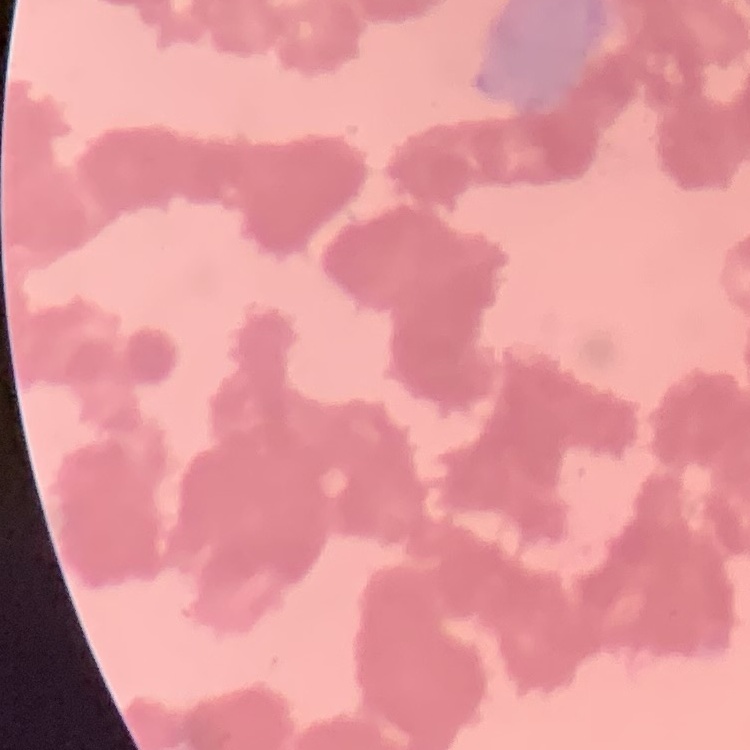

The red blood cells show rouleaux formation. Thin blood film. Stained with either Field's or Giemsa. One tile cut from a larger photomicrograph.